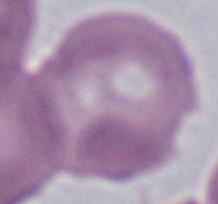 Photomicrograph. A red blood cell is shown. 1000x magnification.